Locate every blood parasite and identify its species.
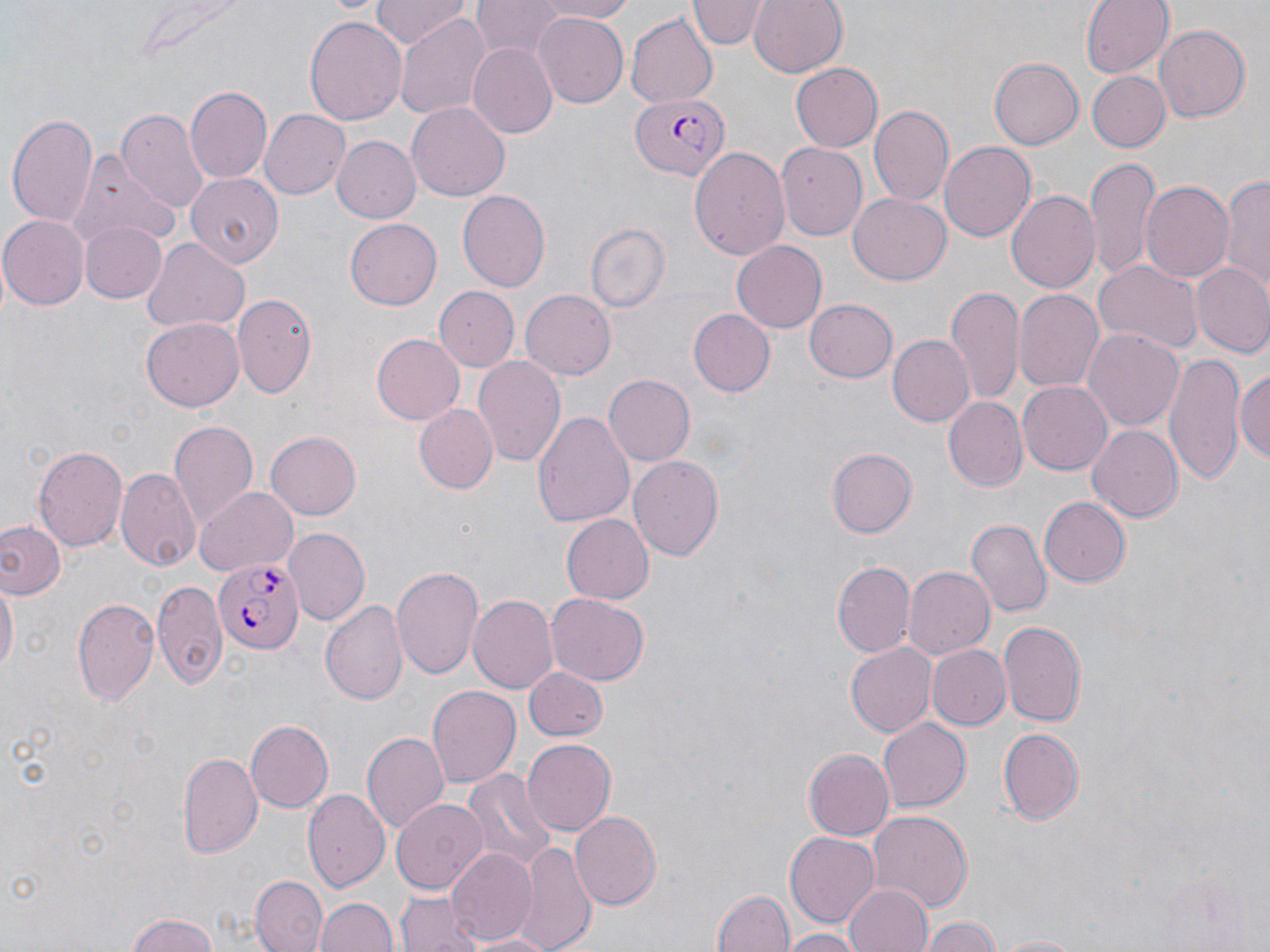
Approximate bounding boxes as [x1, y1, x2, y2] in pixels.
Plasmodium falciparum-infected red blood cells: [628, 93, 726, 180], [215, 555, 307, 652].
No Plasmodium ovale, Plasmodium malariae, Plasmodium vivax, Babesia divergens, or Trypanosoma brucei observed.

Summary:
  - Uninfected red blood cell locations: [325, 0, 388, 17], [371, 0, 470, 49], [530, 0, 639, 22], [687, 0, 766, 49], [748, 0, 848, 78], [1080, 0, 1174, 80], [469, 3, 567, 63], [393, 12, 491, 121], [533, 12, 628, 108], [304, 14, 408, 128], [627, 14, 718, 108], [1153, 25, 1250, 124], [468, 43, 558, 139], [991, 58, 1083, 148], [789, 64, 882, 152], [1087, 72, 1170, 151], [185, 86, 273, 185], [407, 102, 510, 203], [869, 105, 955, 209], [117, 108, 209, 211], [259, 108, 351, 200], [8, 110, 100, 229], [331, 134, 421, 223], [937, 139, 1037, 242], [776, 144, 868, 240], [689, 145, 788, 259], [71, 153, 176, 250], [1085, 158, 1159, 280], [1217, 173, 1270, 303], [187, 174, 284, 267], [1139, 179, 1234, 284], [1006, 188, 1101, 294], [456, 190, 551, 292], [848, 191, 950, 282], [0, 214, 88, 309], [345, 219, 441, 309], [78, 221, 167, 302], [584, 221, 670, 313], [140, 237, 251, 333], [732, 241, 827, 332], [1093, 259, 1202, 356], [1191, 264, 1270, 358], [433, 287, 518, 371], [946, 288, 1024, 405], [521, 290, 616, 380], [1013, 291, 1103, 393], [232, 293, 317, 394], [803, 299, 896, 383], [688, 309, 775, 398], [140, 318, 245, 412], [1083, 326, 1184, 430], [371, 334, 464, 425], [886, 334, 973, 426], [1163, 350, 1245, 486], [474, 356, 566, 468], [1236, 360, 1270, 471], [604, 373, 697, 466], [1018, 383, 1111, 474], [943, 396, 1026, 489], [414, 404, 499, 492], [533, 409, 635, 531], [168, 421, 259, 529], [1088, 424, 1182, 521], [264, 431, 361, 521], [35, 443, 129, 554], [827, 449, 915, 537], [629, 455, 723, 562], [118, 467, 202, 570], [194, 486, 300, 576], [1039, 498, 1131, 587], [561, 514, 654, 603], [966, 520, 1051, 619], [0, 523, 63, 600], [284, 525, 370, 623], [835, 560, 916, 658], [392, 565, 483, 679], [903, 565, 995, 660], [1, 578, 17, 684], [152, 581, 227, 687], [469, 593, 559, 696], [547, 593, 648, 685], [73, 596, 160, 707], [321, 600, 407, 705], [996, 620, 1087, 730], [847, 643, 939, 737], [930, 643, 1010, 731], [523, 667, 607, 742], [426, 685, 521, 789], [878, 718, 971, 811], [245, 720, 334, 810], [996, 725, 1084, 824], [361, 730, 449, 835], [520, 739, 616, 838], [803, 745, 895, 841], [177, 749, 263, 858], [461, 768, 557, 869], [303, 790, 389, 892], [391, 798, 488, 893], [867, 810, 973, 912], [571, 811, 662, 909], [786, 831, 881, 925], [517, 841, 594, 952], [447, 848, 537, 945], [251, 876, 326, 951], [845, 882, 935, 952], [712, 888, 795, 952], [397, 893, 476, 952], [315, 896, 400, 952], [126, 911, 220, 952], [918, 915, 1003, 952], [776, 930, 865, 952], [464, 931, 554, 951], [988, 934, 1093, 951]
  - Slide-level diagnosis: Plasmodium falciparum
  - Image size: 1270×952 pixels
  - Magnification: 1000x
  - Stain: May-Grünwald-Giemsa
  - Preparation: thin blood smear
  - Modality: light microscopy
  - Field of view: single